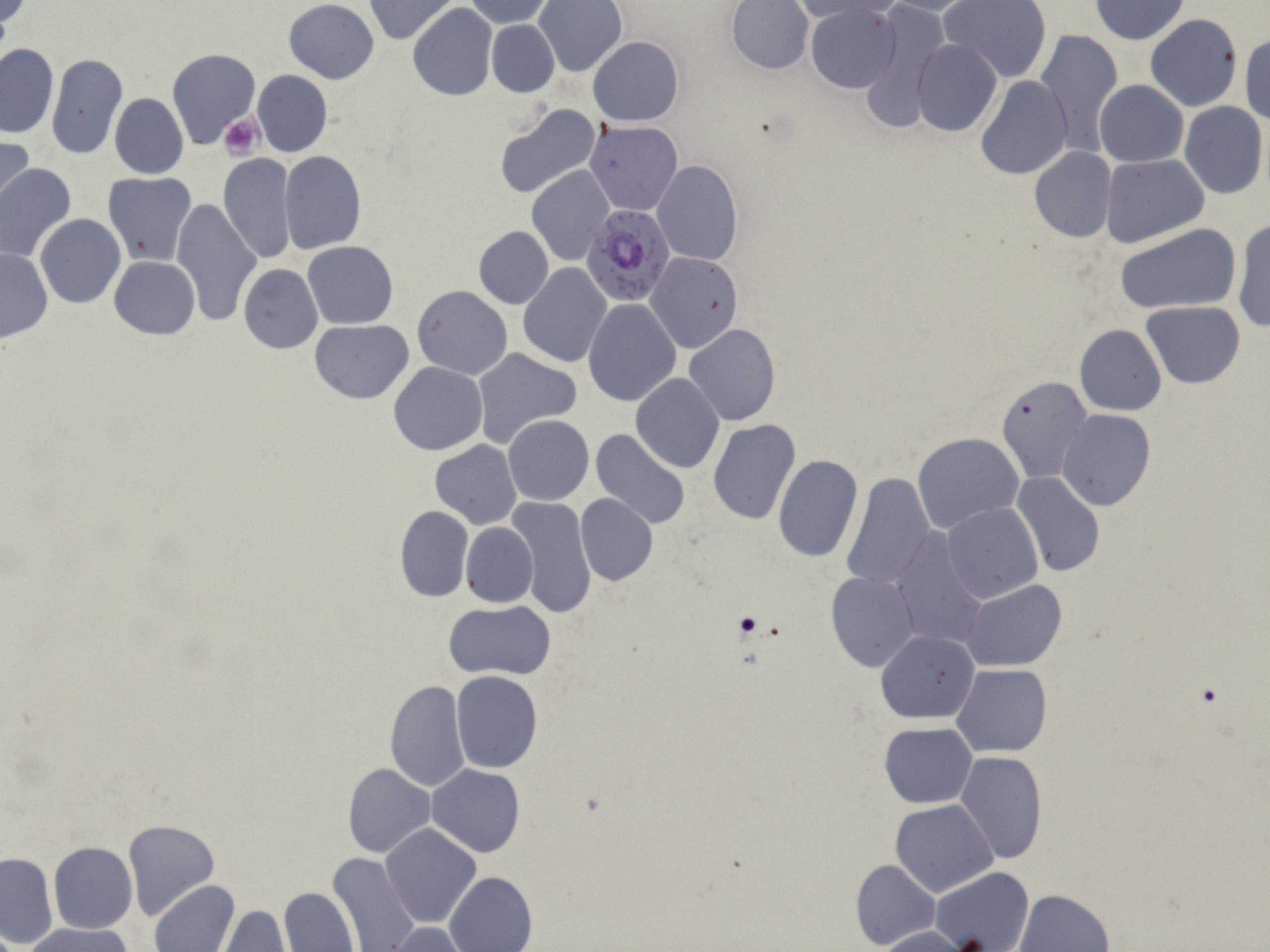

{
  "slide_level_diagnosis": "Plasmodium falciparum",
  "modality": "light microscopy",
  "plasmodium_falciparum_infected_red_blood_cell_locations": "approximate bounding boxes as (x1,y1)-(x2,y2) corner pairs in pixels: (581,203)-(678,306)",
  "field_of_view": "single",
  "stain": "May-Grünwald-Giemsa",
  "image_size": "1270×952 pixels",
  "uninfected_red_blood_cell_locations": "approximate bounding boxes as (x1,y1)-(x2,y2) corner pairs in pixels: (364,0)-(459,43), (466,0)-(554,27), (939,0)-(1052,82), (1091,0)-(1188,44), (536,1)-(626,74), (726,1)-(814,74), (878,1)-(980,15), (283,2)-(379,83), (790,2)-(884,23), (807,4)-(901,93), (408,5)-(498,100), (864,10)-(952,129), (1145,14)-(1242,112), (486,20)-(559,97), (1035,28)-(1124,152), (1241,33)-(1270,126), (587,36)-(684,125), (912,39)-(1002,137), (0,43)-(58,137), (167,49)-(261,149), (47,53)-(127,160), (252,71)-(331,157), (975,76)-(1072,181), (1094,80)-(1188,167), (110,93)-(188,179), (1180,102)-(1268,199), (495,103)-(602,199), (585,120)-(681,216), (0,134)-(34,217), (1028,147)-(1116,242), (279,151)-(366,253), (219,153)-(297,264), (1101,154)-(1208,249), (652,160)-(743,265), (0,161)-(75,263), (527,166)-(615,266), (104,173)-(196,266), (170,201)-(263,323), (36,214)-(126,307), (1231,218)-(1270,334), (1114,223)-(1240,314), (473,226)-(552,308), (304,240)-(398,327), (1,247)-(53,343), (646,252)-(742,355), (109,256)-(200,339), (518,263)-(612,367), (239,264)-(322,353), (413,286)-(512,380), (583,300)-(681,407), (1141,301)-(1246,388), (309,320)-(414,402), (684,324)-(781,427), (1076,325)-(1166,415), (472,348)-(580,448), (389,362)-(488,455), (631,375)-(724,474), (995,375)-(1092,481), (1057,410)-(1155,512), (503,414)-(593,504), (707,420)-(799,524), (589,428)-(691,529), (913,432)-(1025,535), (430,440)-(522,529), (772,455)-(862,563), (842,470)-(933,589), (1010,472)-(1105,580), (576,493)-(657,585), (507,495)-(596,618), (942,503)-(1043,602), (395,505)-(473,601), (461,522)-(538,607), (890,531)-(987,650), (826,571)-(920,672), (960,580)-(1065,672), (444,600)-(556,680), (877,630)-(979,724), (953,664)-(1052,757), (450,671)-(543,773), (383,678)-(470,792), (880,722)-(976,808), (954,752)-(1047,864), (343,763)-(436,858), (427,764)-(525,857), (891,799)-(998,896), (122,819)-(219,921), (382,824)-(481,926), (49,841)-(137,932), (327,851)-(420,952), (1,852)-(56,948), (851,858)-(940,951), (931,866)-(1032,952), (445,871)-(537,952), (150,879)-(239,952), (280,887)-(358,952), (1015,888)-(1114,952), (216,905)-(295,951), (388,923)-(467,952), (29,924)-(130,952), (875,926)-(970,951)",
  "preparation": "thin blood film",
  "magnification": "1000x",
  "platelet_locations": "approximate bounding boxes as (x1,y1)-(x2,y2) corner pairs in pixels: (219,114)-(264,161), (734,610)-(763,638)"
}